State which parasite is depicted.
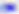

Toxoplasma gondii.

{
  "modality": "micrograph",
  "magnification": "400x"
}